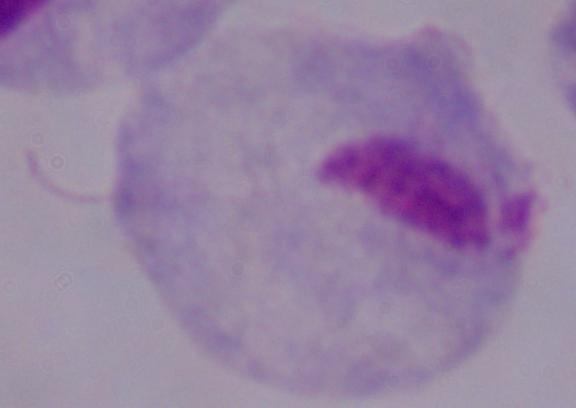
identification: trichomonad
magnification: 1000x
modality: micrograph